Outline each Plasmodium falciparum-infected red blood cell.
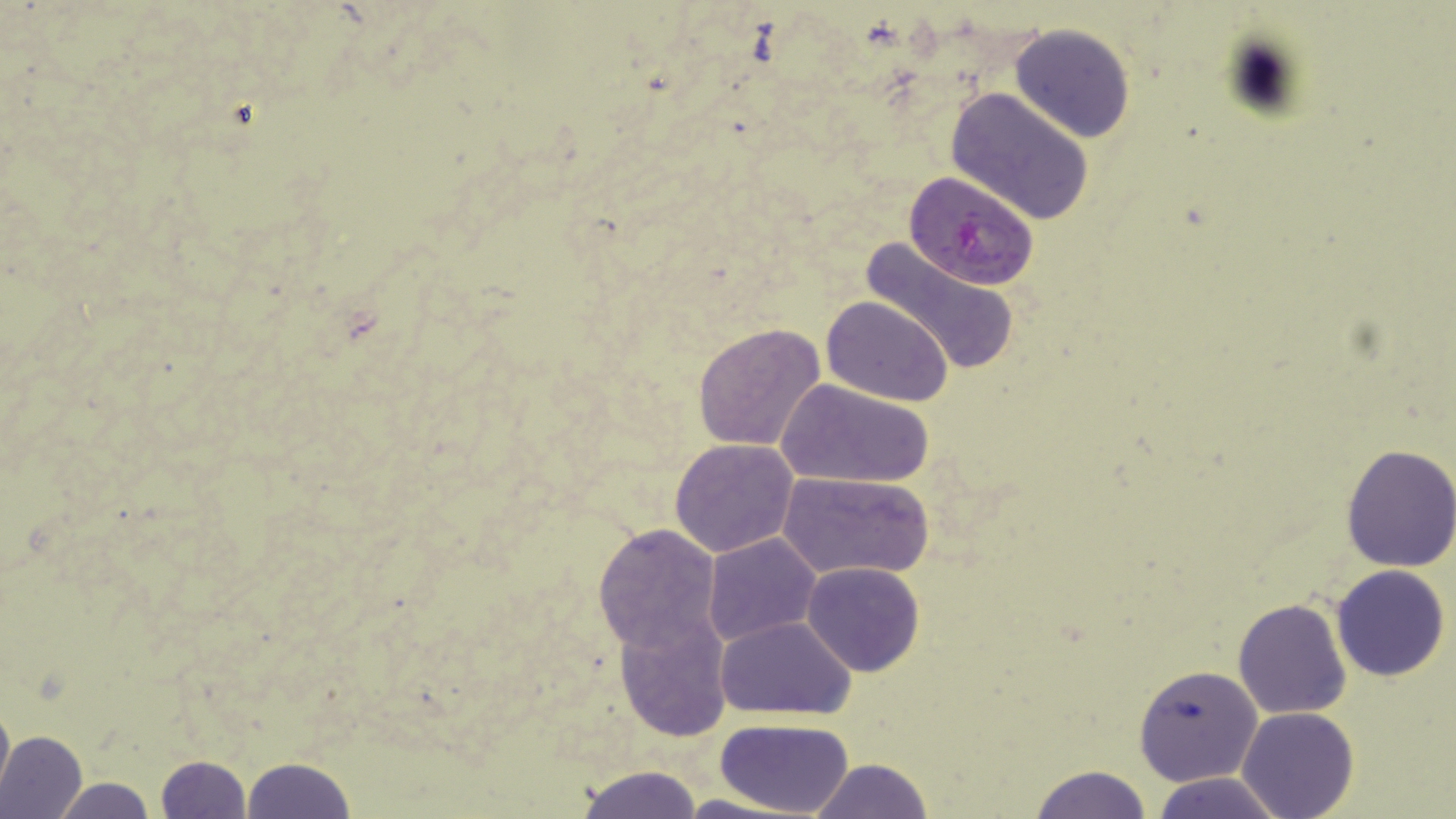

Approximate bounding boxes as [x1, y1, x2, y2] in pixels.
Plasmodium falciparum-infected red blood cells: [904, 170, 1038, 292].

Uninfected red blood cell locations: [1010, 24, 1135, 142], [946, 87, 1093, 222], [860, 237, 1020, 374], [822, 295, 952, 404], [692, 324, 826, 452], [778, 380, 933, 489], [670, 438, 799, 556], [1338, 444, 1456, 573], [779, 471, 932, 582], [592, 524, 723, 654], [702, 533, 821, 647], [802, 561, 925, 677], [1332, 564, 1451, 682], [1232, 598, 1355, 719], [616, 612, 732, 740], [715, 614, 856, 720], [1134, 663, 1263, 786], [0, 695, 13, 807], [1236, 707, 1360, 819], [715, 719, 854, 818], [0, 729, 87, 819], [155, 754, 252, 819], [241, 757, 357, 818], [809, 758, 933, 818], [573, 765, 703, 818], [1030, 765, 1153, 819], [1151, 771, 1289, 819], [50, 777, 158, 818], [667, 794, 803, 819]. Slide-level diagnosis: Plasmodium falciparum. 1000x magnification. Single field of view. Light microscopy. May-Grünwald-Giemsa stain. Thin blood smear. Image is 1456×819 pixels.